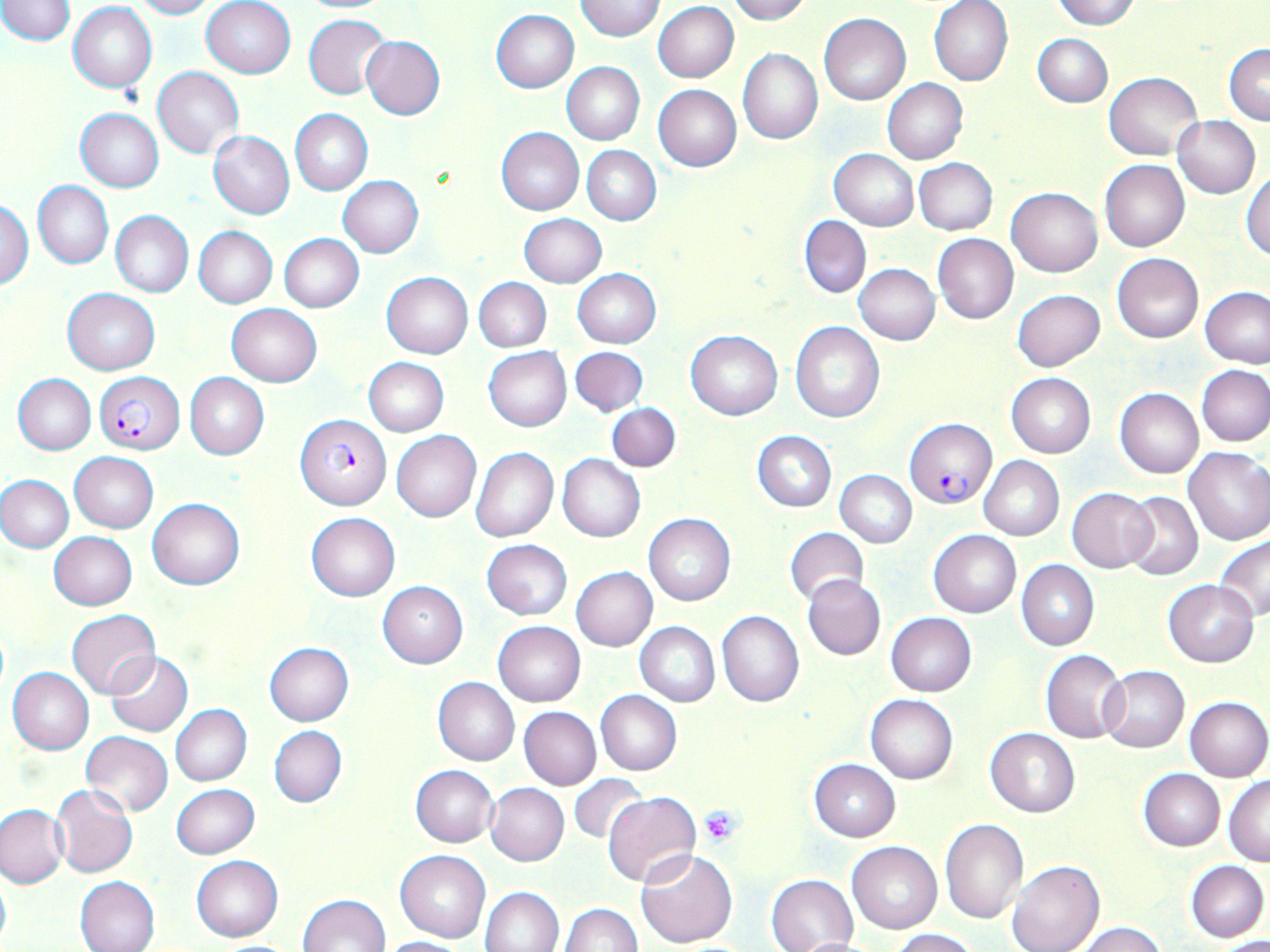

Summary:
  - Coordinate format: approximate bounding boxes as (x1, y1, x2, y2) in pixels
  - Uninfected red blood cell locations: (0, 0, 74, 45), (132, 0, 217, 19), (574, 0, 666, 41), (726, 0, 808, 24), (1051, 0, 1141, 30), (201, 1, 296, 78), (929, 1, 1014, 86), (69, 2, 158, 93), (652, 2, 739, 83), (492, 10, 579, 92), (818, 13, 911, 105), (304, 14, 391, 100), (1033, 33, 1113, 107), (360, 35, 445, 119), (1225, 44, 1270, 125), (738, 48, 823, 144), (561, 62, 646, 145), (152, 67, 244, 158), (1105, 72, 1201, 159), (881, 78, 968, 165), (653, 84, 742, 171), (75, 109, 163, 192), (290, 109, 371, 195), (1173, 115, 1260, 198), (497, 127, 584, 215), (208, 131, 294, 219), (582, 146, 661, 224), (829, 149, 918, 230), (915, 158, 997, 235), (925, 159, 1005, 321), (1100, 159, 1190, 251), (1243, 170, 1270, 261), (338, 176, 424, 257), (33, 181, 113, 270), (1006, 187, 1102, 277), (1, 199, 33, 289), (110, 210, 193, 298), (519, 215, 606, 287), (799, 215, 871, 298), (194, 226, 278, 308), (278, 234, 364, 312), (932, 234, 1019, 324), (1111, 252, 1204, 343), (853, 264, 939, 345), (572, 269, 661, 349), (381, 273, 473, 358), (475, 278, 550, 350), (1199, 286, 1269, 369), (63, 287, 159, 375), (1012, 289, 1105, 371), (227, 303, 321, 387), (791, 323, 884, 422), (686, 331, 782, 419), (570, 346, 648, 417), (484, 347, 571, 431), (363, 358, 448, 437), (1196, 364, 1270, 447), (184, 373, 268, 460), (1006, 373, 1095, 458), (12, 374, 95, 456), (1115, 387, 1204, 478), (608, 403, 681, 472), (391, 431, 480, 523), (752, 431, 837, 511), (1183, 447, 1270, 545), (471, 448, 558, 542), (70, 452, 159, 533), (557, 455, 645, 542), (979, 455, 1064, 540), (835, 469, 917, 546), (0, 473, 74, 554), (1066, 487, 1158, 573), (1121, 491, 1203, 581), (147, 498, 244, 590), (306, 513, 400, 601), (643, 513, 735, 606), (785, 528, 869, 607), (929, 530, 1021, 617), (49, 532, 137, 609), (1215, 534, 1270, 620), (482, 539, 572, 619), (1017, 560, 1099, 650), (570, 566, 657, 651), (803, 575, 886, 661), (1163, 580, 1258, 667), (378, 581, 467, 667), (67, 609, 159, 698), (716, 611, 803, 707), (886, 613, 977, 695), (493, 621, 585, 706), (634, 622, 719, 706), (264, 642, 354, 725), (1040, 650, 1127, 743), (105, 651, 194, 738), (1100, 666, 1189, 753), (8, 667, 94, 754), (433, 677, 520, 765), (596, 691, 681, 776), (865, 694, 958, 784), (1184, 696, 1269, 780), (170, 704, 251, 785), (519, 707, 600, 791), (268, 724, 347, 808), (985, 727, 1080, 818), (81, 732, 173, 816), (809, 759, 900, 842), (411, 765, 498, 847), (1138, 770, 1225, 851), (567, 774, 647, 846), (1225, 776, 1270, 865), (52, 783, 137, 878), (486, 783, 569, 865), (171, 784, 259, 858), (602, 790, 701, 887), (0, 804, 68, 887), (939, 818, 1028, 924), (847, 841, 941, 933), (634, 848, 739, 948), (395, 850, 489, 943), (192, 855, 283, 941), (1008, 860, 1104, 952), (1185, 860, 1268, 942), (0, 866, 11, 950), (766, 873, 858, 952), (74, 875, 160, 952), (481, 886, 565, 952), (299, 893, 390, 952), (559, 903, 641, 952), (1076, 922, 1165, 952), (888, 928, 978, 951), (1211, 935, 1270, 952), (379, 936, 467, 952), (789, 936, 885, 952)
  - Plasmodium falciparum-infected red blood cell locations: (95, 371, 184, 454), (296, 414, 391, 511), (904, 419, 996, 508)
  - Platelet locations: (699, 806, 741, 845)
  - Slide-level diagnosis: Plasmodium falciparum
  - Field of view: one of a larger specimen
  - Magnification: 1000x
  - Preparation: thin blood smear
  - Modality: light microscopy
  - Image size: 1270×952 pixels
  - Stain: May-Grünwald-Giemsa